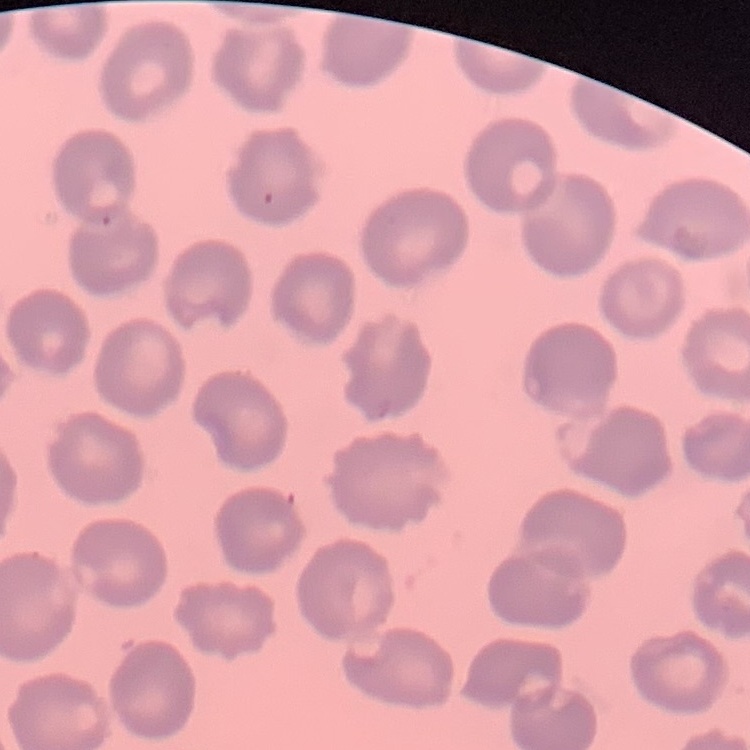 The erythrocytes exhibit no rouleaux formation. One tile cut from a larger photomicrograph. Stained with either Field's or Giemsa. Thin peripheral smear.